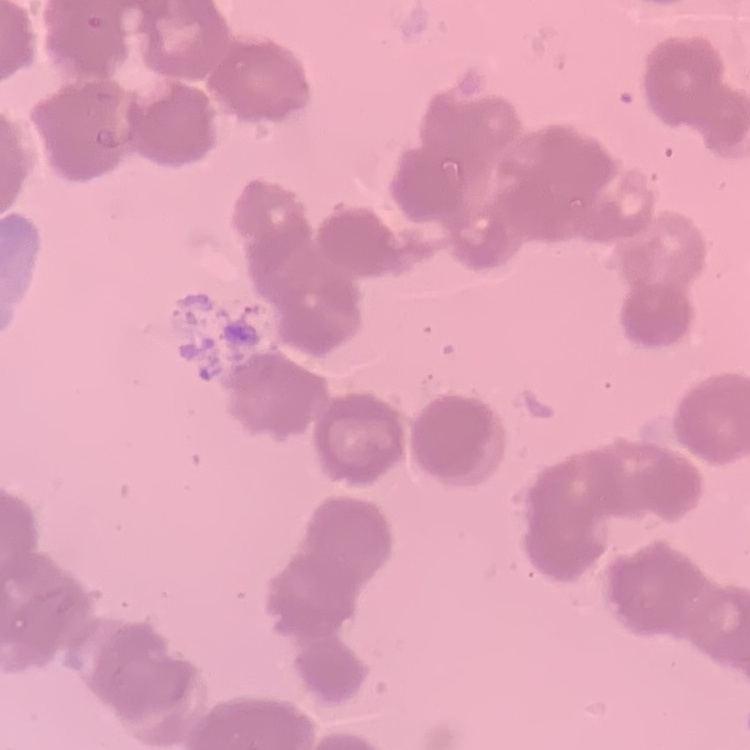
Summary:
  - Erythrocyte morphology: rouleaux formation
  - Preparation: thin blood smear
  - Stain: Field's or Giemsa
  - Image type: square crop of a larger photomicrograph